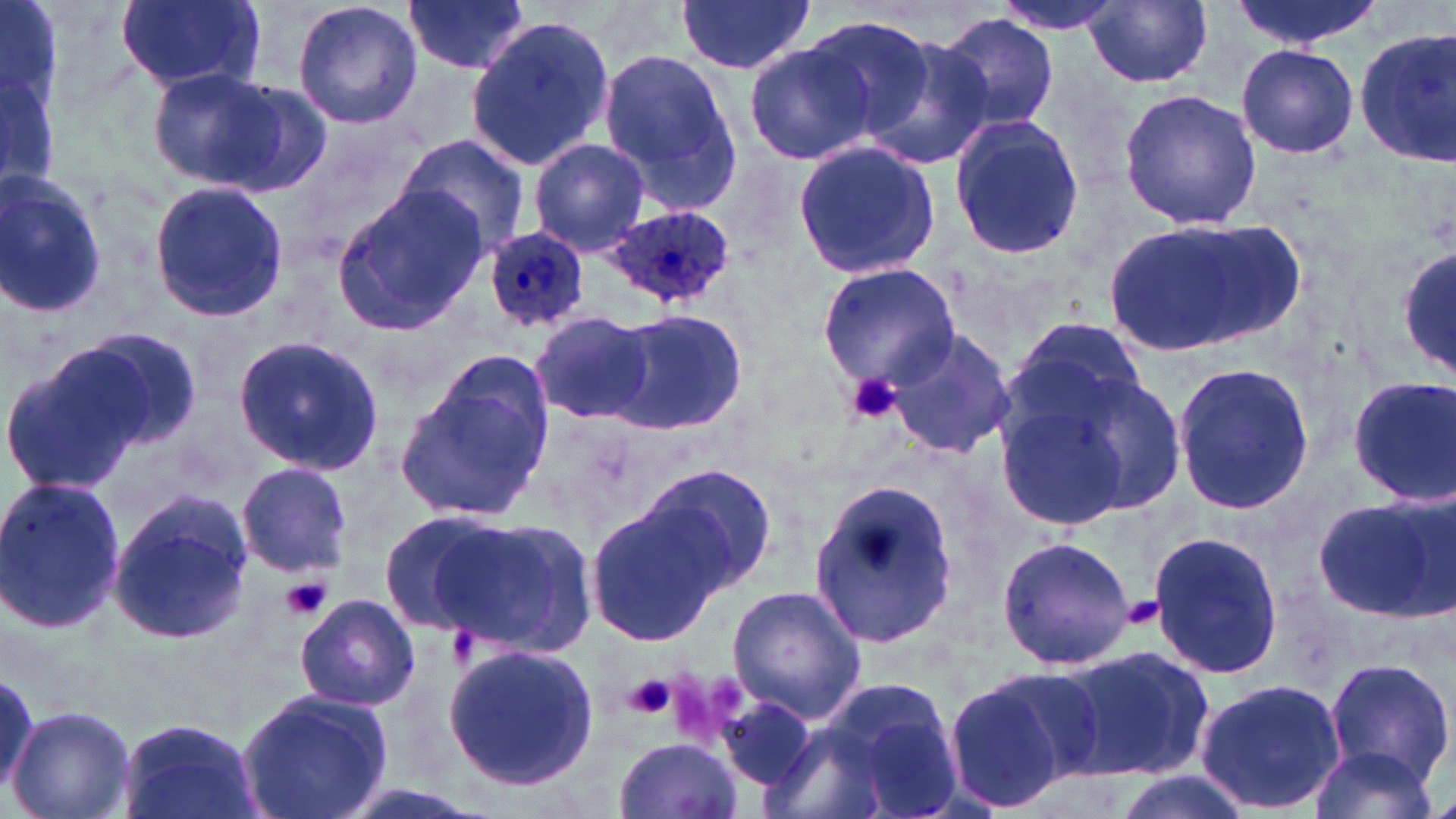
slide-level diagnosis = Plasmodium ovale
preparation = thin blood smear
field of view = one of a larger specimen
image size = 1456×819 pixels
platelet locations = approximate bounding boxes as named x1/y1/x2/y2 corners in pixels: (x1=844, y1=372, x2=906, y2=426), (x1=281, y1=578, x2=330, y2=621), (x1=1120, y1=597, x2=1163, y2=631), (x1=706, y1=672, x2=749, y2=714), (x1=670, y1=673, x2=719, y2=747), (x1=621, y1=674, x2=677, y2=720)
Plasmodium ovale-infected red blood cell locations = approximate bounding boxes as named x1/y1/x2/y2 corners in pixels: (x1=601, y1=205, x2=734, y2=308), (x1=479, y1=227, x2=590, y2=332)
modality = light microscopy
stain = May-Grünwald-Giemsa
magnification = 1000x
uninfected red blood cell locations = approximate bounding boxes as named x1/y1/x2/y2 corners in pixels: (x1=115, y1=0, x2=262, y2=93), (x1=292, y1=0, x2=422, y2=130), (x1=402, y1=0, x2=530, y2=74), (x1=674, y1=0, x2=814, y2=74), (x1=988, y1=0, x2=1129, y2=34), (x1=1227, y1=0, x2=1387, y2=52), (x1=1087, y1=1, x2=1212, y2=87), (x1=0, y1=13, x2=61, y2=194), (x1=937, y1=13, x2=1060, y2=136), (x1=465, y1=16, x2=615, y2=172), (x1=799, y1=16, x2=937, y2=137), (x1=856, y1=28, x2=996, y2=166), (x1=1352, y1=28, x2=1456, y2=165), (x1=746, y1=43, x2=875, y2=165), (x1=1236, y1=44, x2=1359, y2=160), (x1=596, y1=45, x2=742, y2=216), (x1=151, y1=67, x2=309, y2=192), (x1=1118, y1=88, x2=1262, y2=232), (x1=949, y1=115, x2=1084, y2=258), (x1=399, y1=135, x2=529, y2=256), (x1=529, y1=137, x2=650, y2=257), (x1=791, y1=138, x2=942, y2=281), (x1=0, y1=169, x2=107, y2=321), (x1=148, y1=181, x2=289, y2=323), (x1=332, y1=187, x2=488, y2=327), (x1=1099, y1=218, x2=1294, y2=360), (x1=1396, y1=248, x2=1456, y2=380), (x1=815, y1=262, x2=961, y2=393), (x1=608, y1=308, x2=746, y2=435), (x1=528, y1=309, x2=654, y2=425), (x1=76, y1=327, x2=203, y2=448), (x1=884, y1=329, x2=1017, y2=458), (x1=232, y1=336, x2=385, y2=474), (x1=982, y1=338, x2=1172, y2=528), (x1=0, y1=348, x2=153, y2=496), (x1=397, y1=357, x2=553, y2=525), (x1=1172, y1=362, x2=1317, y2=516), (x1=1346, y1=375, x2=1456, y2=505), (x1=235, y1=461, x2=352, y2=577), (x1=646, y1=465, x2=776, y2=589), (x1=0, y1=475, x2=124, y2=636), (x1=808, y1=481, x2=963, y2=650), (x1=106, y1=487, x2=254, y2=648), (x1=1315, y1=493, x2=1456, y2=623), (x1=586, y1=502, x2=727, y2=647), (x1=380, y1=510, x2=511, y2=634), (x1=435, y1=516, x2=598, y2=658), (x1=1147, y1=529, x2=1283, y2=683), (x1=995, y1=533, x2=1136, y2=671), (x1=726, y1=585, x2=866, y2=721), (x1=295, y1=592, x2=418, y2=711), (x1=442, y1=641, x2=599, y2=789), (x1=1053, y1=642, x2=1214, y2=785), (x1=1322, y1=657, x2=1454, y2=791), (x1=945, y1=670, x2=1096, y2=813), (x1=0, y1=674, x2=46, y2=801), (x1=1195, y1=676, x2=1346, y2=816), (x1=825, y1=678, x2=964, y2=814), (x1=236, y1=689, x2=395, y2=819), (x1=720, y1=695, x2=816, y2=791), (x1=7, y1=705, x2=135, y2=819), (x1=115, y1=714, x2=262, y2=819), (x1=614, y1=736, x2=743, y2=818), (x1=1307, y1=743, x2=1439, y2=819), (x1=1104, y1=769, x2=1252, y2=819), (x1=324, y1=782, x2=490, y2=819)